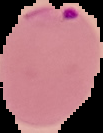
Cell region segmented out of the field of view; the surrounding area is masked to black. Image is 103×133 pixels. Malaria status: parasitized. From a thin blood film.